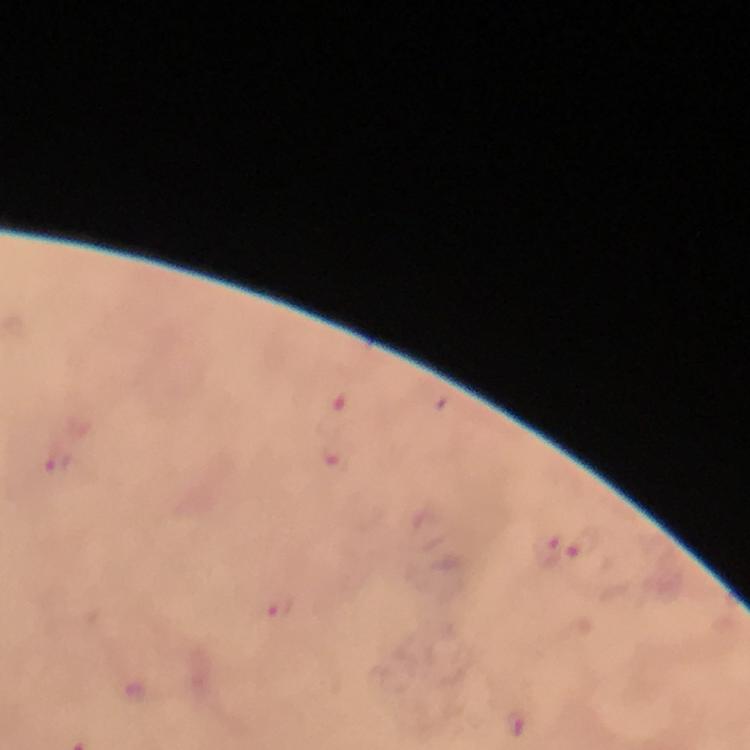 Approximate centers as [x, y] in pixels. Malaria parasite locations: [342, 404], [335, 459], [60, 461], [582, 543], [548, 548], [279, 609]. Giemsa stain. At 100x magnification. Immersion oil was used. From a malaria diagnostic workup. Smartphone photograph taken through a microscope. Thick blood film. A crop from one field of view. Image is 750×750 pixels.